Name the parasite shown.
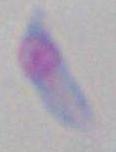
This is Toxoplasma gondii.

Micrograph. Captured at 1000x magnification.